Classify this cell by malaria status.
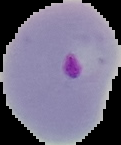
It is parasitized.

Summary:
  - Image type: cell region segmented out of the field of view; surrounding area masked to black
  - Image size: 121×145 pixels
  - Preparation: thin blood film